Assess this cell for malaria.
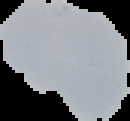
It is uninfected.

Segmented cell region on a black background. Image is 130×121 pixels. From a thin blood film.